Outline each Plasmodium malariae-infected red blood cell.
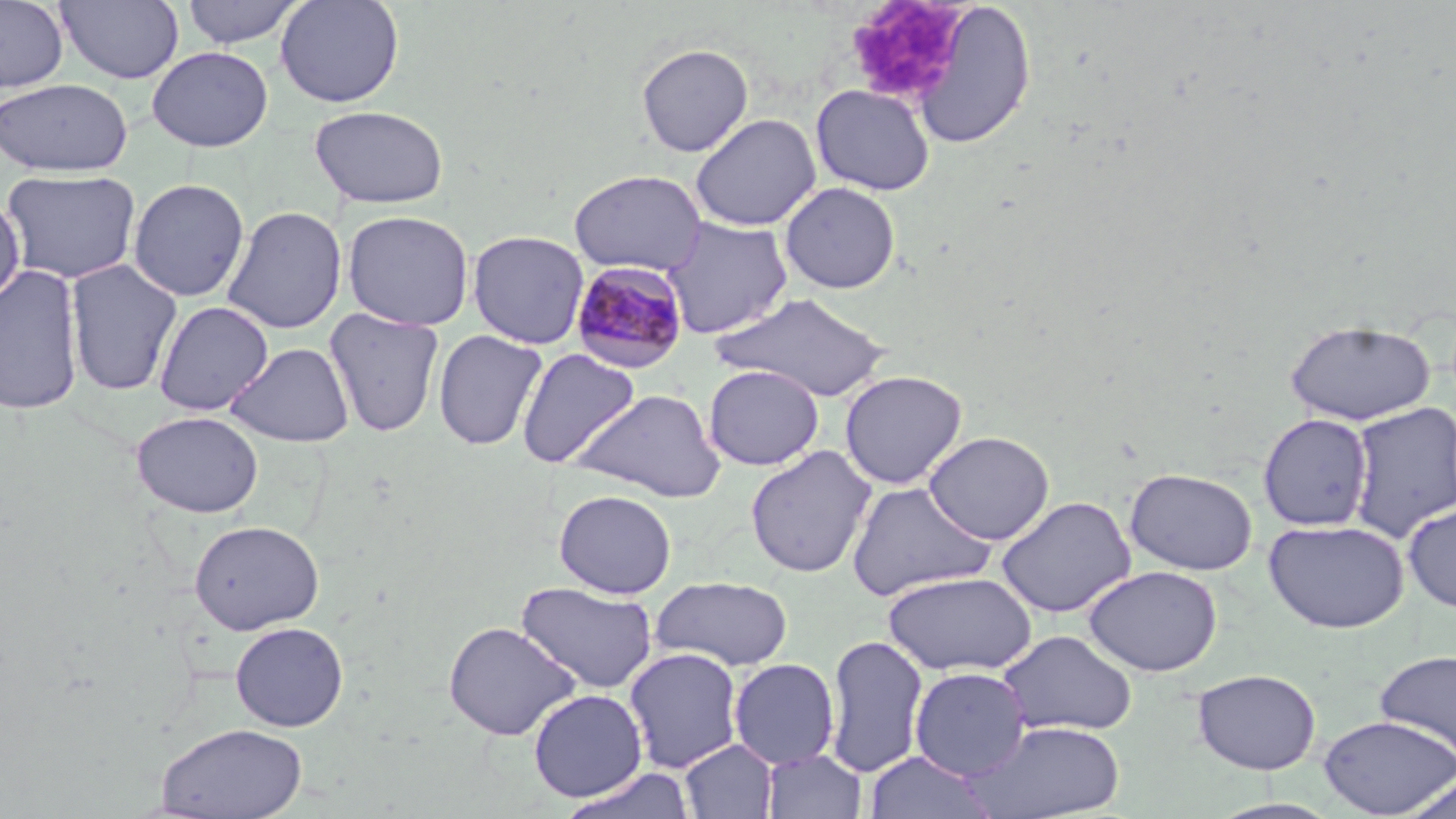
Approximate bounding boxes as named x1/y1/x2/y2 corners in pixels.
Plasmodium malariae-infected red blood cells: (x1=570, y1=260, x2=690, y2=375).

Uninfected red blood cell locations: (x1=0, y1=0, x2=69, y2=93), (x1=56, y1=0, x2=185, y2=85), (x1=179, y1=0, x2=308, y2=49), (x1=275, y1=0, x2=405, y2=107), (x1=907, y1=2, x2=1038, y2=150), (x1=636, y1=43, x2=754, y2=157), (x1=147, y1=46, x2=273, y2=151), (x1=0, y1=78, x2=133, y2=177), (x1=810, y1=84, x2=936, y2=196), (x1=310, y1=104, x2=448, y2=209), (x1=690, y1=113, x2=821, y2=232), (x1=3, y1=169, x2=141, y2=284), (x1=568, y1=169, x2=707, y2=276), (x1=128, y1=178, x2=250, y2=302), (x1=779, y1=182, x2=901, y2=294), (x1=0, y1=193, x2=25, y2=310), (x1=222, y1=205, x2=348, y2=334), (x1=341, y1=209, x2=475, y2=331), (x1=660, y1=216, x2=793, y2=339), (x1=467, y1=229, x2=590, y2=349), (x1=64, y1=259, x2=183, y2=396), (x1=0, y1=263, x2=85, y2=417), (x1=713, y1=293, x2=892, y2=401), (x1=153, y1=300, x2=274, y2=416), (x1=324, y1=307, x2=445, y2=437), (x1=1284, y1=319, x2=1436, y2=426), (x1=432, y1=329, x2=547, y2=450), (x1=226, y1=342, x2=354, y2=447), (x1=516, y1=348, x2=640, y2=469), (x1=703, y1=364, x2=824, y2=470), (x1=839, y1=369, x2=968, y2=489), (x1=569, y1=387, x2=726, y2=502), (x1=1348, y1=401, x2=1456, y2=542), (x1=131, y1=410, x2=264, y2=518), (x1=1258, y1=413, x2=1373, y2=531), (x1=923, y1=430, x2=1055, y2=545), (x1=745, y1=445, x2=877, y2=578), (x1=1124, y1=467, x2=1258, y2=575), (x1=846, y1=481, x2=996, y2=601), (x1=554, y1=489, x2=677, y2=598), (x1=996, y1=495, x2=1137, y2=618), (x1=1402, y1=502, x2=1456, y2=614), (x1=189, y1=519, x2=325, y2=635), (x1=1263, y1=519, x2=1409, y2=633), (x1=1084, y1=565, x2=1222, y2=677), (x1=883, y1=570, x2=1038, y2=676), (x1=651, y1=575, x2=793, y2=670), (x1=637, y1=577, x2=772, y2=757), (x1=516, y1=581, x2=659, y2=694), (x1=442, y1=620, x2=581, y2=741), (x1=230, y1=621, x2=349, y2=732), (x1=997, y1=630, x2=1138, y2=736), (x1=823, y1=633, x2=929, y2=778), (x1=624, y1=646, x2=744, y2=774), (x1=1374, y1=650, x2=1456, y2=765), (x1=728, y1=657, x2=840, y2=769), (x1=909, y1=666, x2=1031, y2=780), (x1=1192, y1=668, x2=1321, y2=775), (x1=528, y1=689, x2=648, y2=802), (x1=1318, y1=714, x2=1455, y2=818), (x1=970, y1=719, x2=1126, y2=819), (x1=155, y1=721, x2=309, y2=819), (x1=680, y1=739, x2=778, y2=819), (x1=761, y1=748, x2=867, y2=819), (x1=864, y1=751, x2=997, y2=819), (x1=558, y1=766, x2=697, y2=819), (x1=1400, y1=775, x2=1456, y2=819), (x1=1208, y1=798, x2=1343, y2=819). Platelet locations: (x1=843, y1=0, x2=970, y2=105). Slide-level diagnosis: Plasmodium malariae. Thin blood smear. Light microscopy. Single field of view. Image is 1456×819 pixels. Captured at 1000x magnification. May-Grünwald-Giemsa-stained preparation.